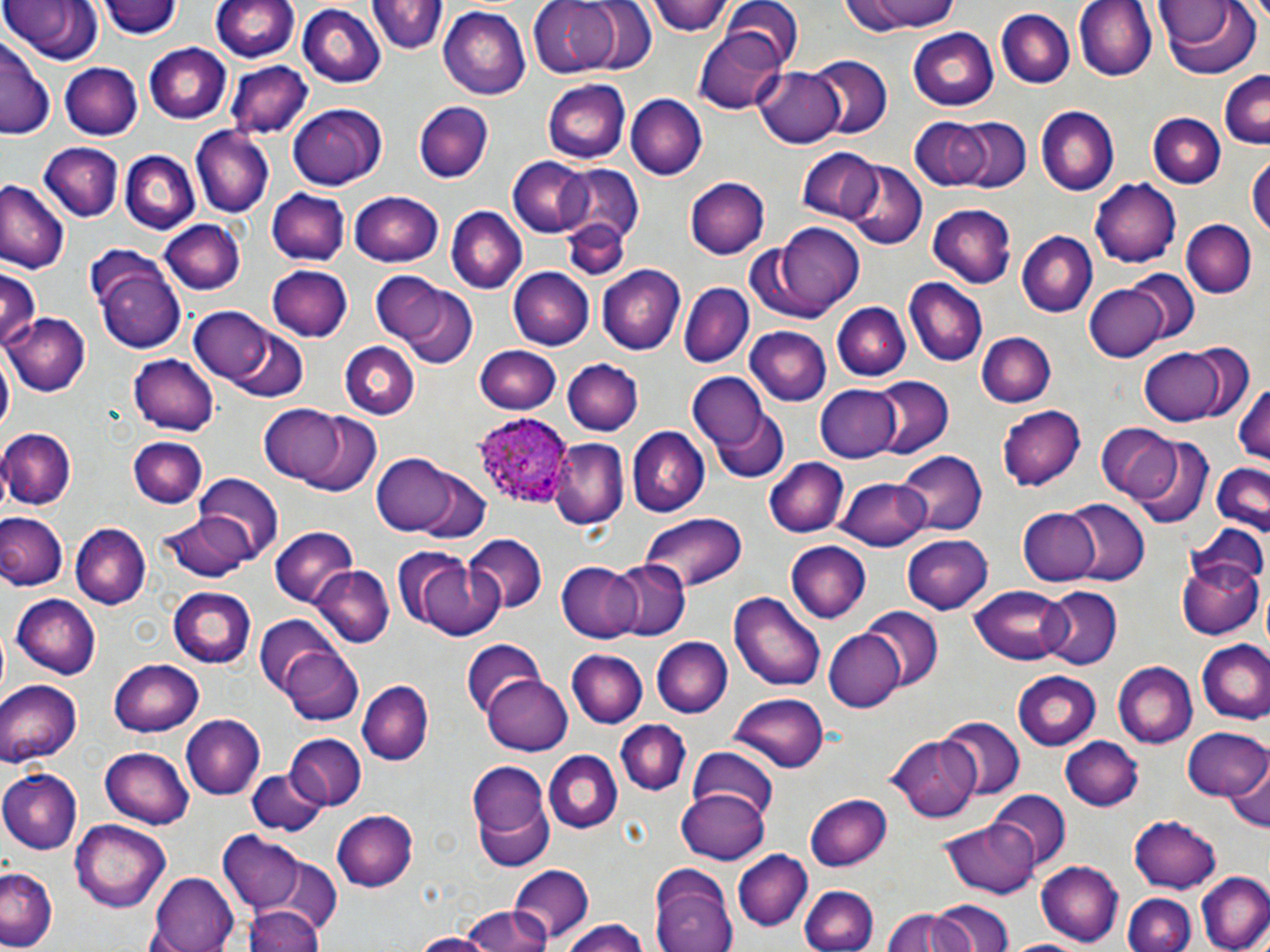
slide_level_diagnosis: Plasmodium ovale
image_size: 1270×952 pixels
field_of_view: one of a larger specimen
plasmodium_ovale_infected_red_blood_cell_locations: 'approximate bounding boxes as [x1, y1, x2, y2] in pixels: [475, 416, 572, 507]'
modality: light microscopy
stain: May-Grünwald-Giemsa
magnification: 1000x
uninfected_red_blood_cell_locations: 'approximate bounding boxes as [x1, y1, x2, y2] in pixels: [4, 0, 112, 65], [102, 0, 182, 40], [212, 0, 298, 63], [529, 0, 626, 78], [569, 0, 657, 75], [650, 0, 732, 38], [717, 0, 806, 71], [839, 0, 961, 34], [1075, 0, 1157, 81], [369, 2, 445, 58], [1159, 2, 1262, 80], [296, 4, 385, 86], [437, 7, 529, 101], [996, 9, 1076, 90], [910, 27, 1002, 111], [693, 28, 789, 113], [0, 38, 53, 140], [145, 43, 232, 124], [806, 57, 891, 140], [60, 62, 144, 139], [228, 62, 312, 139], [756, 67, 846, 148], [1217, 70, 1270, 147], [543, 78, 630, 162], [625, 94, 706, 179], [413, 100, 493, 181], [287, 101, 388, 191], [1035, 106, 1119, 196], [951, 114, 1032, 194], [1148, 114, 1223, 189], [909, 116, 995, 189], [191, 128, 273, 215], [43, 142, 122, 222], [122, 147, 201, 233], [796, 149, 882, 222], [1247, 154, 1269, 245], [509, 156, 594, 237], [841, 160, 927, 249], [554, 163, 646, 244], [685, 176, 769, 261], [1090, 176, 1181, 265], [0, 183, 68, 274], [268, 189, 348, 266], [350, 191, 445, 266], [930, 203, 1015, 286], [445, 206, 526, 294], [1182, 219, 1256, 297], [158, 220, 244, 296], [560, 220, 627, 280], [772, 222, 869, 313], [1016, 232, 1096, 318], [86, 249, 186, 353], [266, 264, 354, 343], [597, 265, 685, 354], [509, 267, 594, 349], [0, 268, 39, 355], [1127, 269, 1201, 346], [374, 273, 455, 349], [901, 278, 987, 368], [680, 283, 752, 368], [1085, 283, 1166, 362], [396, 286, 478, 368], [830, 301, 908, 382], [187, 308, 275, 383], [6, 314, 89, 396], [220, 324, 309, 403], [743, 327, 831, 405], [977, 332, 1056, 408], [340, 341, 420, 419], [474, 344, 562, 414], [1137, 345, 1237, 427], [0, 352, 13, 438], [129, 355, 217, 434], [562, 356, 645, 435], [687, 373, 765, 452], [869, 377, 952, 458], [1232, 379, 1270, 467], [815, 385, 904, 462], [261, 402, 353, 485], [996, 404, 1084, 491], [713, 409, 790, 484], [296, 411, 385, 498], [1097, 425, 1180, 502], [0, 427, 76, 509], [627, 427, 708, 517], [1129, 434, 1212, 527], [128, 436, 207, 509], [554, 438, 629, 529], [899, 450, 986, 537], [371, 452, 463, 536], [766, 458, 847, 538], [1208, 463, 1270, 535], [408, 467, 493, 546], [193, 475, 284, 561], [838, 476, 930, 551], [1061, 500, 1149, 587], [1017, 507, 1100, 586], [0, 512, 67, 591], [159, 513, 255, 583], [638, 513, 745, 593], [70, 523, 148, 609], [1187, 523, 1270, 600], [269, 528, 358, 608], [902, 534, 993, 614], [462, 535, 546, 616], [787, 542, 871, 623], [413, 554, 501, 639], [1177, 556, 1262, 642], [606, 559, 691, 640], [556, 562, 640, 642], [314, 566, 392, 647], [971, 584, 1072, 663], [170, 586, 256, 667], [1038, 586, 1122, 668], [732, 592, 826, 691], [10, 594, 99, 678], [862, 608, 942, 689], [254, 619, 339, 698], [824, 629, 904, 713], [650, 637, 732, 719], [460, 641, 545, 718], [1198, 641, 1270, 724], [279, 646, 365, 727], [568, 650, 647, 729], [108, 657, 203, 736], [1113, 662, 1196, 748], [1011, 671, 1101, 751], [483, 674, 573, 756], [0, 679, 80, 768], [356, 680, 431, 767], [731, 692, 830, 770], [181, 715, 264, 799], [936, 715, 1025, 799], [618, 719, 691, 797], [1184, 728, 1270, 805], [284, 734, 367, 810], [887, 736, 980, 819], [1060, 737, 1145, 811], [101, 746, 195, 826], [686, 746, 779, 820], [544, 751, 622, 834], [1225, 756, 1270, 837], [469, 761, 554, 866], [0, 769, 80, 854], [245, 770, 327, 835], [676, 787, 770, 864], [991, 790, 1071, 867], [805, 792, 892, 871], [330, 809, 417, 893], [1127, 814, 1222, 892], [940, 816, 1041, 897], [71, 820, 170, 910], [219, 833, 305, 912], [733, 850, 811, 931], [246, 860, 341, 942], [1036, 861, 1123, 944], [508, 862, 594, 946], [0, 866, 58, 948], [651, 868, 737, 952], [151, 871, 241, 952], [1195, 871, 1269, 952], [799, 884, 879, 952], [1124, 894, 1195, 951], [936, 901, 1014, 952], [245, 905, 323, 952], [460, 906, 548, 952], [882, 909, 962, 952], [557, 918, 654, 951], [407, 932, 496, 952], [1007, 936, 1094, 952]'
preparation: thin blood smear